Report the malaria status of this cell.
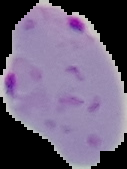
Parasitized.

From a thin blood film. Segmented cell region on a black background. Image is 127×169 pixels.